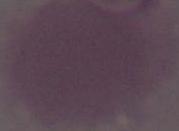

Summary:
  - Modality: photomicrograph
  - Magnification: 1000x
  - Identification: erythrocyte